Assess the morphology of the red blood cells.
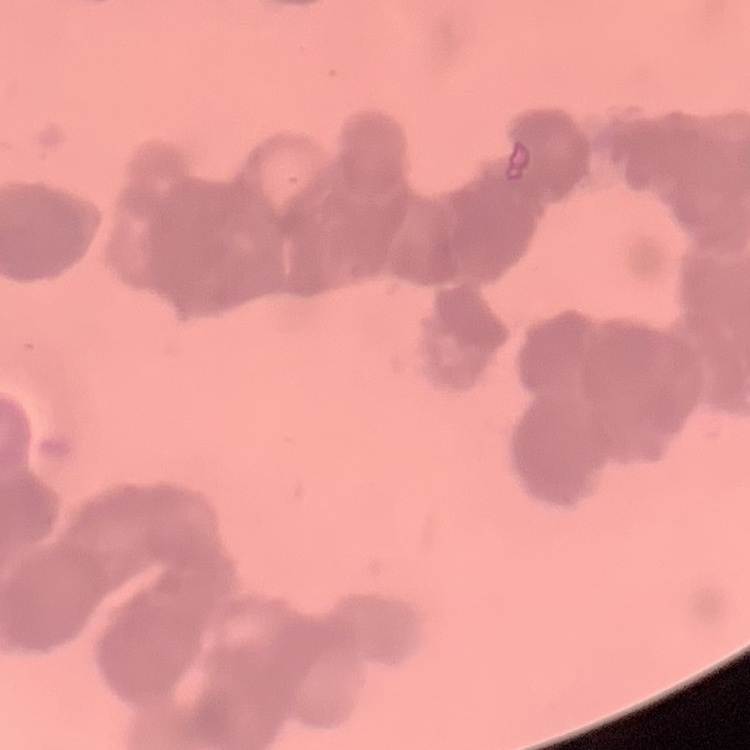

Rouleaux formation.

Thin peripheral smear. One tile cut from a larger photomicrograph. Stained with either Field's or Giemsa.